Classify this cell by malaria status.
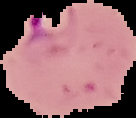
Parasitized.

Image is 136×118 pixels. Segmented cell region on a black background. From a thin blood smear.